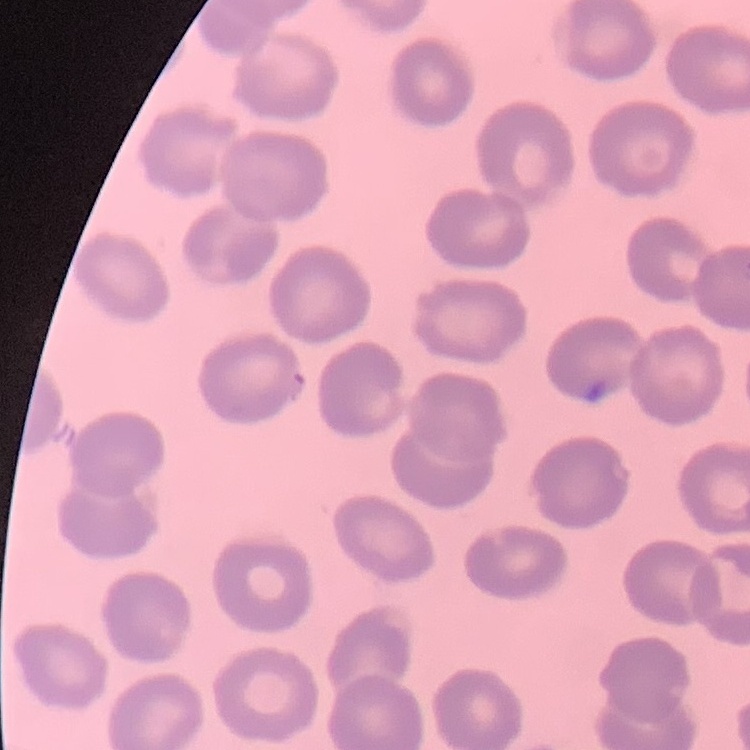
red_blood_cell_morphology: no rouleaux formation
image_type: square crop of a larger photomicrograph
preparation: thin blood film
stain: Field's or Giemsa